Assess this cell for malaria.
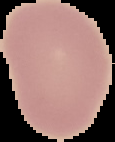
Uninfected.

image size = 115×142 pixels
image type = segmented cell region with the area outside set to black
preparation = thin blood film